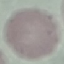

result = negative for malaria parasites
preparation = thin blood smear
capture = smartphone camera at the microscope eyepiece
image type = automatically extracted cell patch, resized to 64 × 64 pixels
stain = Giemsa